Name the parasite shown.
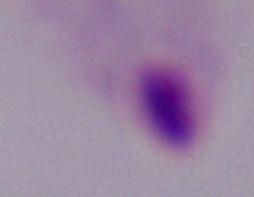
This is a trichomonad.

Summary:
  - Modality: micrograph
  - Magnification: 1000x